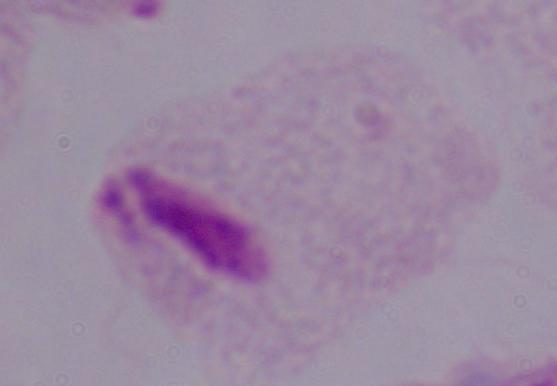
Summary:
  - Identification: trichomonad
  - Modality: micrograph
  - Magnification: 1000x